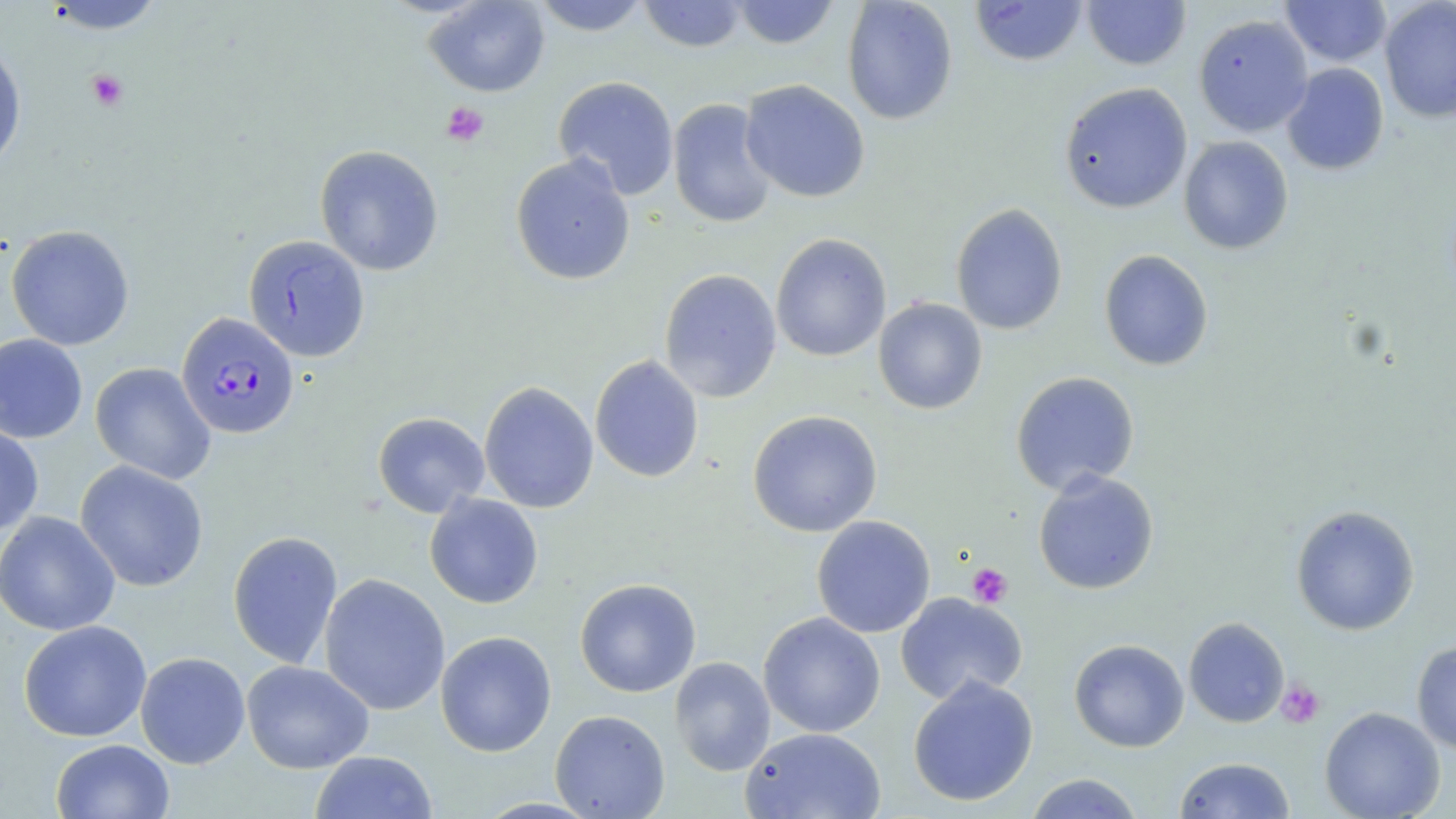

Approximate bounding boxes as [x1, y1, x2, y2] in pixels. Platelet locations: [86, 69, 129, 112], [441, 101, 489, 146], [968, 563, 1013, 608], [1276, 680, 1325, 728]. Uninfected red blood cell locations: [424, 0, 550, 97], [531, 0, 653, 36], [636, 0, 748, 52], [727, 0, 841, 49], [841, 0, 958, 125], [970, 0, 1088, 66], [1082, 0, 1191, 70], [41, 1, 167, 36], [1279, 1, 1392, 67], [1379, 1, 1456, 124], [1193, 14, 1313, 137], [0, 40, 27, 175], [1281, 63, 1389, 176], [552, 76, 679, 200], [740, 79, 870, 203], [1059, 82, 1193, 214], [667, 98, 778, 229], [1178, 136, 1294, 255], [314, 145, 444, 276], [510, 154, 635, 286], [951, 202, 1068, 335], [6, 224, 135, 350], [771, 233, 891, 362], [243, 234, 370, 362], [1099, 249, 1214, 371], [659, 268, 782, 403], [873, 297, 988, 415], [0, 333, 88, 443], [589, 355, 704, 483], [90, 362, 216, 485], [1010, 371, 1140, 495], [479, 381, 598, 513], [747, 410, 883, 537], [373, 412, 489, 518], [0, 421, 43, 536], [75, 460, 209, 592], [1033, 470, 1159, 595], [425, 493, 543, 609], [1290, 505, 1420, 635], [0, 510, 121, 636], [812, 515, 935, 638], [227, 530, 343, 668], [319, 573, 450, 715], [574, 577, 702, 698], [895, 592, 1028, 704], [758, 612, 886, 737], [1183, 617, 1289, 728], [18, 620, 152, 742], [435, 630, 557, 757], [1069, 638, 1189, 752], [1411, 640, 1456, 755], [135, 651, 250, 769], [669, 656, 776, 776], [241, 660, 374, 773], [907, 675, 1039, 807], [1320, 706, 1445, 819], [550, 709, 670, 818], [741, 726, 886, 819], [50, 739, 175, 819], [310, 750, 438, 819], [1174, 757, 1296, 818], [1023, 773, 1146, 818]. Plasmodium falciparum-infected red blood cell locations: [175, 312, 300, 439]. Slide-level diagnosis: Plasmodium falciparum. Image is 1456×819 pixels. Captured at 1000x magnification. Light microscopy. Thin blood film. Single field of view. May-Grünwald-Giemsa-stained preparation.